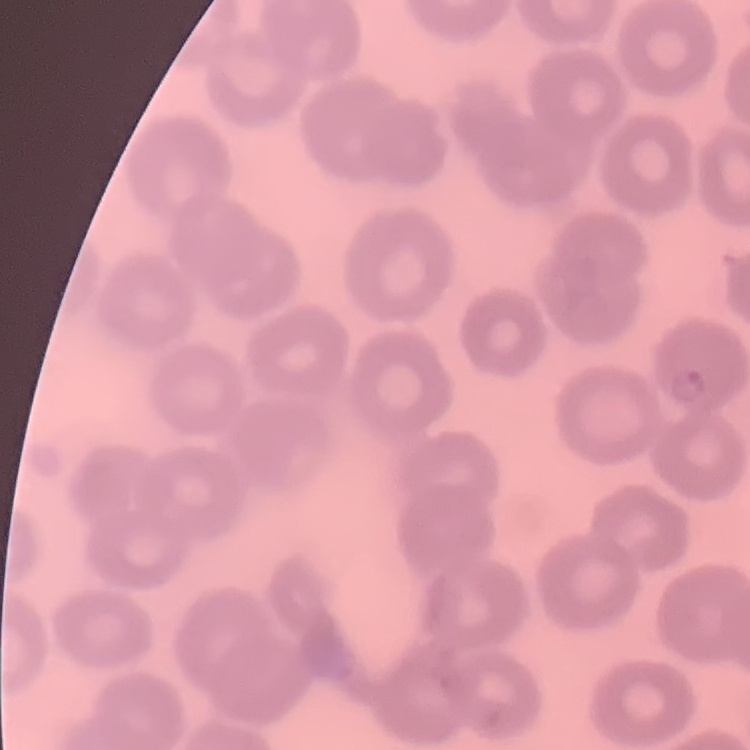
The red blood cells exhibit no rouleaux formation. Square crop of a larger photomicrograph. Stained with either Field's or Giemsa. Thin peripheral smear.